Identify the parasite.
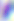
Toxoplasma gondii.

magnification = 400x
modality = photomicrograph